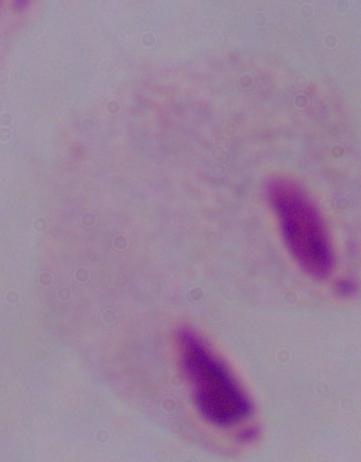

Summary:
  - Modality: micrograph
  - Magnification: 1000x
  - Identification: trichomonad